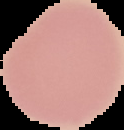 Segmented cell region on a black background. Image is 124×130 pixels. From a thin blood film. Result: no Plasmodium parasites seen.